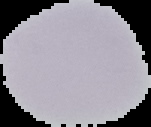

{
  "result": "negative for Plasmodium parasites",
  "image_size": "151×127 pixels",
  "image_type": "segmented cell region on a black background",
  "preparation": "thin blood film"
}